Assess this cell for malaria.
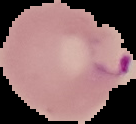
Parasitized.

Summary:
  - Image size: 136×124 pixels
  - Preparation: thin blood film
  - Image type: cell region segmented out of the field of view; surrounding area masked to black